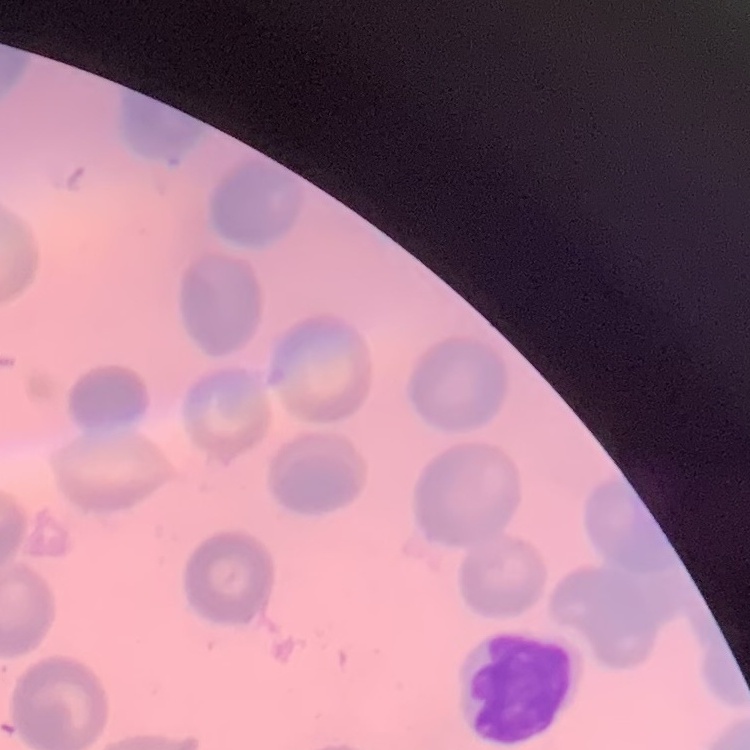

The erythrocytes show no rouleaux formation. Square crop of a larger photomicrograph. Thin peripheral smear. Field's or Giemsa stain.